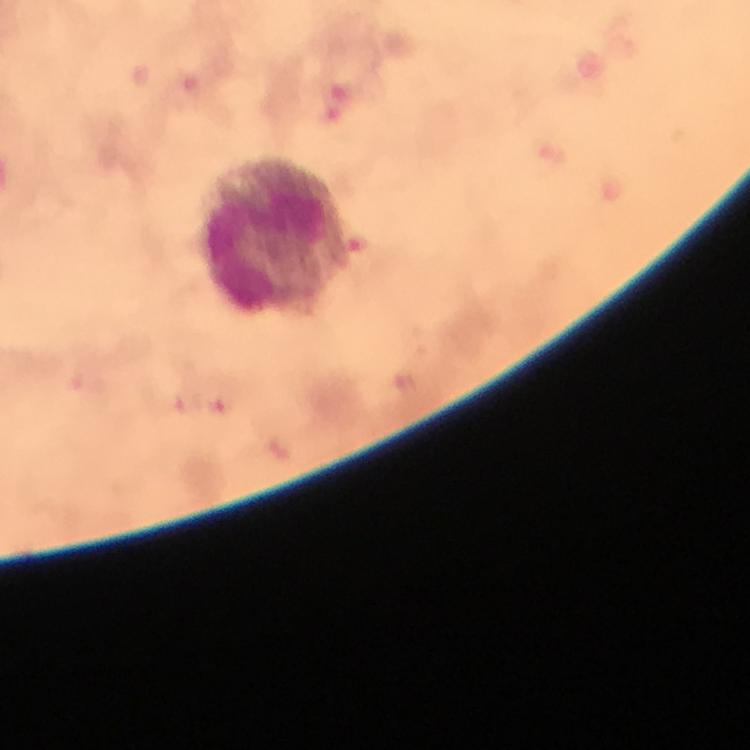

Approximate centers as (x, y) in pixels. Plasmodium parasite locations: (225, 408). Leukocyte locations: (275, 238). Smartphone photograph taken through a microscope. Thick smear. A crop from one field of view. From a diagnostic examination for malaria. Immersion oil was used. Giemsa stain. Image is 750×750 pixels. At 100x magnification.